Describe the morphology of the erythrocytes.
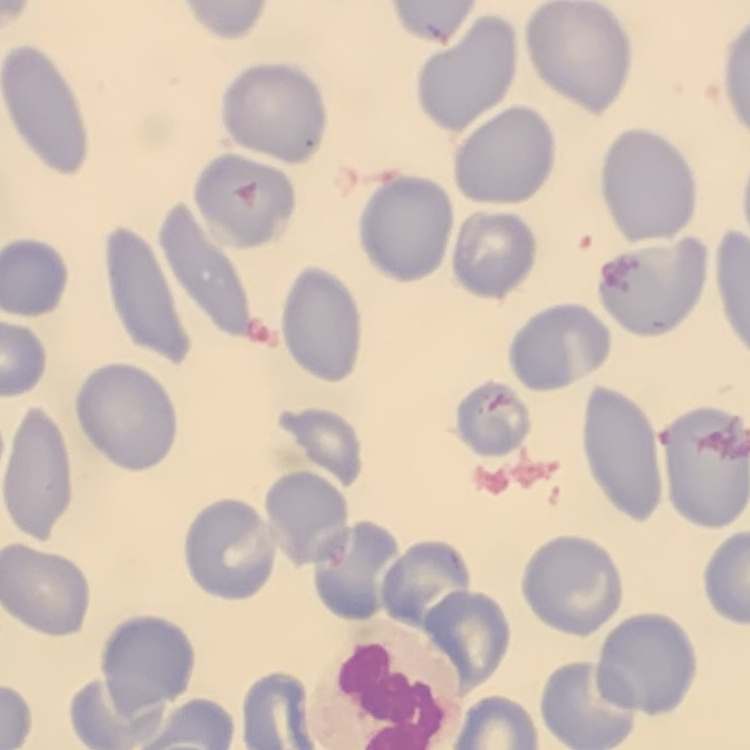

They show no rouleaux formation.

stain = Field's or Giemsa
image type = one tile cut from a larger photomicrograph
preparation = thin peripheral smear